Locate the cells, classifying each as a parasitized red blood cell, an uninfected red blood cell, or a white blood cell.
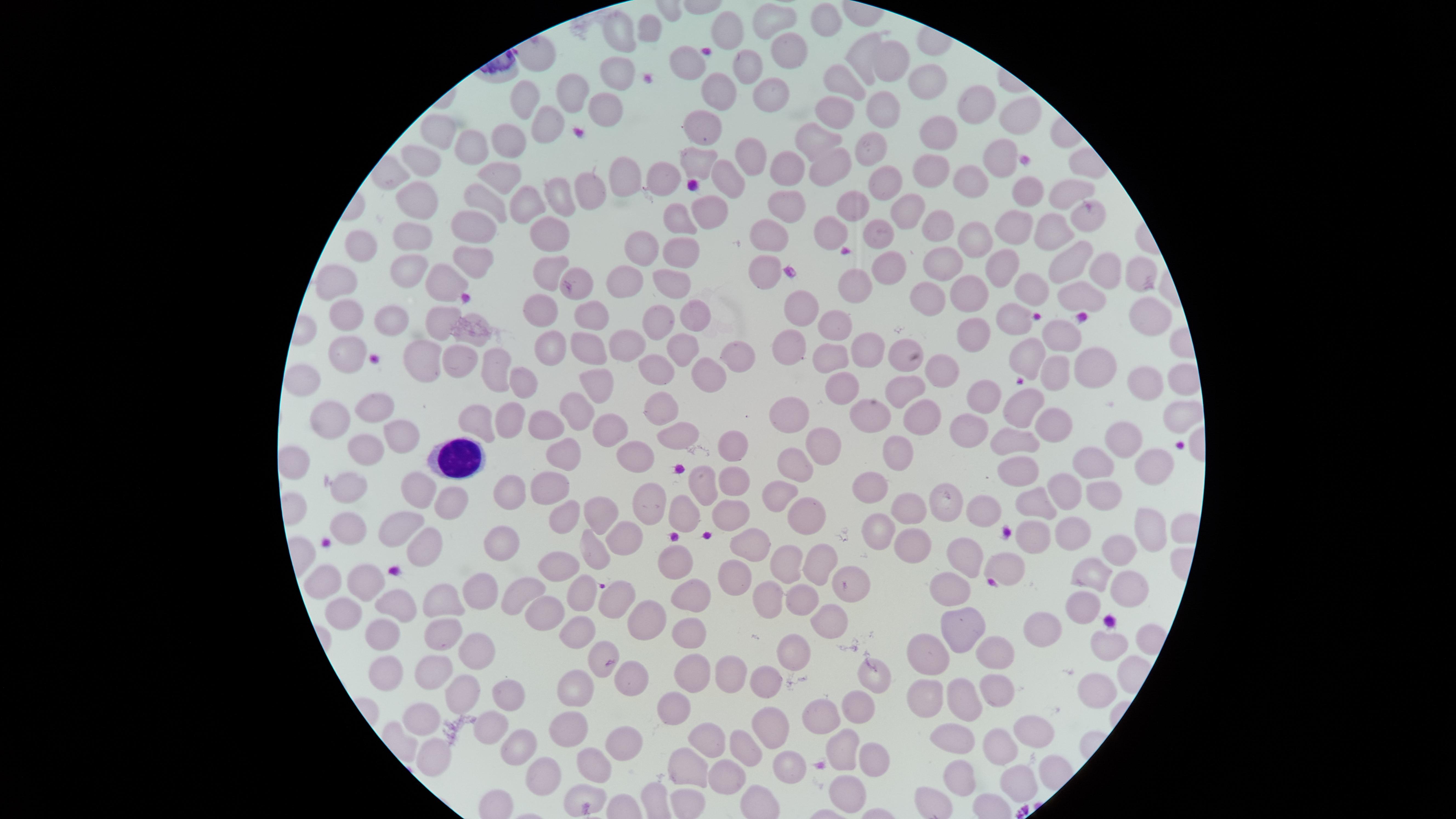

No parasitized red blood cells identified.
Approximate marker points as [x, y] in pixels.
Uninfected red blood cells: [613, 23], [771, 23], [646, 26], [733, 27], [830, 27], [790, 51], [862, 57], [891, 58], [687, 65], [742, 66], [624, 73], [927, 77], [840, 80], [715, 82], [575, 90], [769, 94], [523, 97], [976, 105], [837, 106], [877, 106], [611, 109], [1017, 119], [542, 120], [702, 127], [934, 131], [444, 136], [511, 140], [822, 143], [480, 147], [868, 147], [998, 155], [747, 158], [690, 163], [424, 164], [619, 167], [788, 168], [836, 169], [931, 174], [498, 177], [659, 179], [965, 180], [727, 181], [877, 185], [590, 189], [417, 191], [1066, 191], [1027, 193], [552, 194], [523, 203], [785, 205], [852, 207], [486, 208], [705, 210], [912, 213], [1085, 220], [938, 223], [1011, 225], [474, 227], [680, 227], [839, 230], [415, 232], [873, 232], [1049, 233], [552, 234], [971, 236], [768, 239], [365, 244], [640, 244], [675, 254], [473, 259], [1072, 261], [406, 266], [944, 266], [547, 267], [760, 268], [890, 268], [1001, 268], [1103, 270], [579, 277], [623, 277], [1136, 277], [340, 280], [670, 280], [439, 281], [856, 285], [1031, 288], [969, 294], [1077, 294], [932, 295], [802, 307], [538, 310], [1143, 311], [690, 312], [1013, 315], [347, 316], [442, 317], [656, 318], [394, 319], [590, 319], [835, 323], [979, 333], [1056, 333], [477, 335], [631, 338], [791, 340], [585, 345], [547, 346], [863, 349], [343, 351], [680, 351], [419, 352], [1031, 354], [903, 356], [831, 358], [459, 360], [727, 360], [492, 369], [656, 369], [1055, 369], [1096, 369], [942, 371], [305, 378], [519, 379], [702, 379], [599, 381], [904, 383], [1148, 383], [844, 386], [977, 392], [668, 402], [577, 404], [1013, 406], [373, 410], [511, 411], [923, 412], [789, 414], [478, 415], [866, 417], [1050, 419], [332, 420], [544, 422], [606, 422], [966, 427], [1016, 428], [680, 431], [397, 435], [821, 436], [1124, 436], [733, 440], [568, 444], [362, 450], [628, 455], [896, 456], [290, 462], [1148, 464], [1091, 465], [796, 466], [1013, 466], [727, 480], [870, 480], [347, 483], [701, 484], [1063, 488], [407, 490], [541, 491], [1097, 492], [779, 493], [509, 494], [1028, 499], [655, 501], [941, 501], [441, 502], [911, 502], [982, 508], [601, 509], [800, 509], [568, 513], [727, 513], [683, 518], [397, 526], [343, 528], [1147, 528], [875, 533], [624, 534], [1031, 534], [1073, 536], [909, 542], [421, 544], [590, 546], [756, 546], [1115, 547], [501, 549], [955, 554], [676, 559], [553, 560], [1006, 561], [814, 562], [785, 568], [1087, 569], [738, 575], [328, 576], [851, 581], [365, 583], [1127, 586], [472, 589], [575, 589], [686, 591], [953, 592], [514, 594], [765, 599], [437, 601], [608, 601], [801, 603], [1076, 605], [398, 606], [347, 610], [541, 610], [645, 615], [831, 619], [962, 623], [580, 627], [437, 630], [1049, 633], [385, 635], [690, 635], [1107, 638], [469, 647], [791, 648], [931, 653], [1003, 653], [597, 659], [392, 666], [430, 668], [693, 673], [732, 673], [633, 679], [874, 679], [768, 682], [1095, 689], [995, 693], [455, 694], [571, 694], [919, 694], [959, 695], [499, 699], [672, 707], [849, 707], [826, 714], [423, 715], [771, 721], [563, 727], [491, 732], [1027, 732], [949, 736], [622, 741], [706, 742], [844, 743], [514, 744], [741, 745], [995, 747], [434, 752], [870, 757], [586, 763], [784, 763], [689, 771], [541, 774], [968, 776], [1018, 778], [722, 779], [849, 794], [582, 799].
White blood cells: [456, 458].

field_of_view: single
capture: smartphone photograph through the microscope eyepiece
visible_region: circular
preparation: thin blood film
image_size: 1456×819 pixels
stain: Giemsa